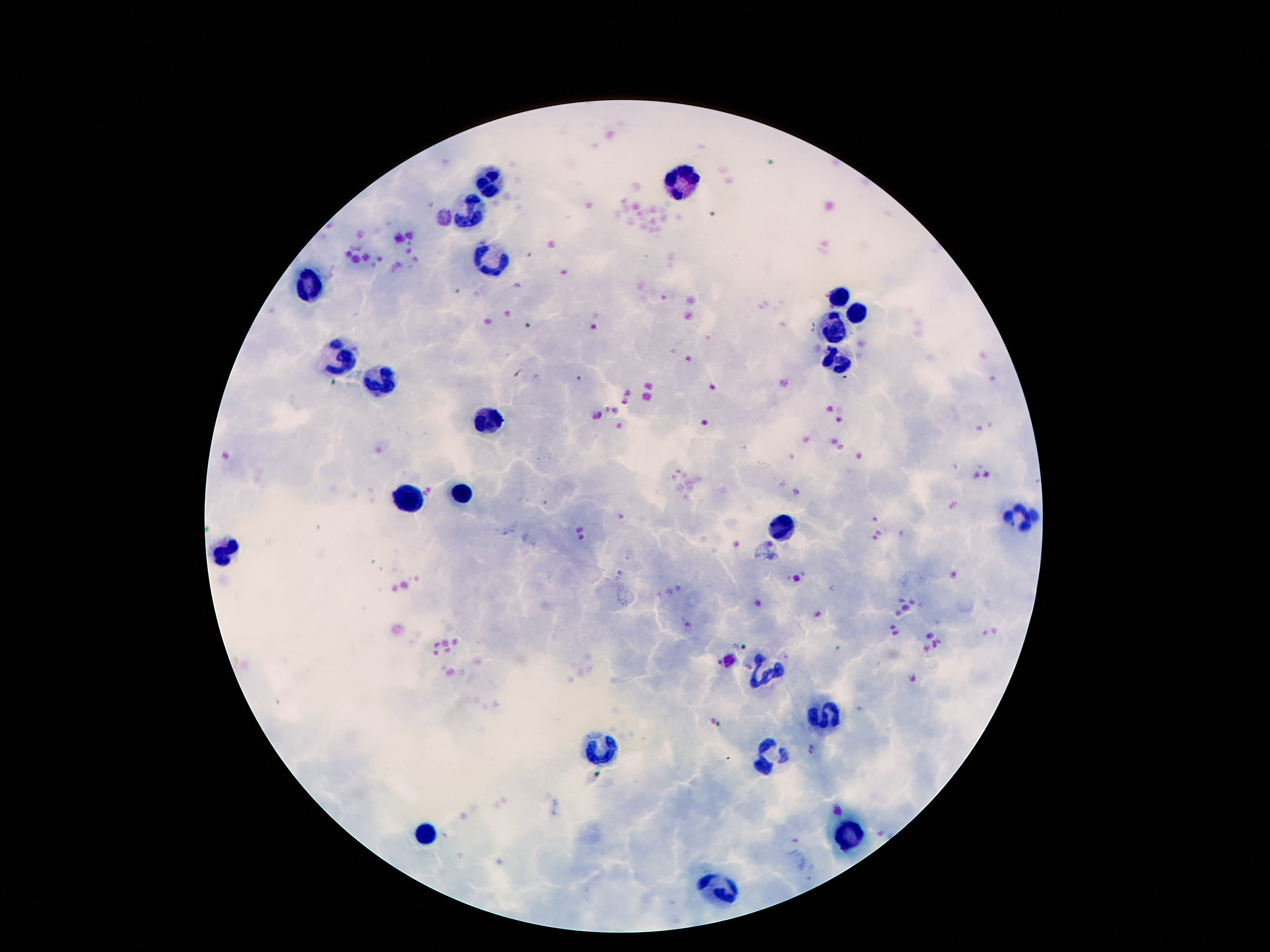
capture = smartphone camera through the microscope eyepiece
patient malaria status = uninfected
leukocyte locations = approximate centers as (x, y) in pixels: (488, 180), (687, 180), (472, 210), (492, 258), (312, 286), (840, 296), (857, 316), (834, 329), (341, 348), (834, 361), (375, 380), (486, 421), (462, 493), (408, 501), (1012, 516), (781, 528), (224, 551), (763, 672), (822, 716), (605, 748), (767, 756), (849, 832), (423, 833), (717, 887)
image size = 1270×952 pixels
field of view = one from this slide
magnification = 100x
preparation = thick peripheral-blood smear
stain = Giemsa